Locate every blood parasite and identify its species.
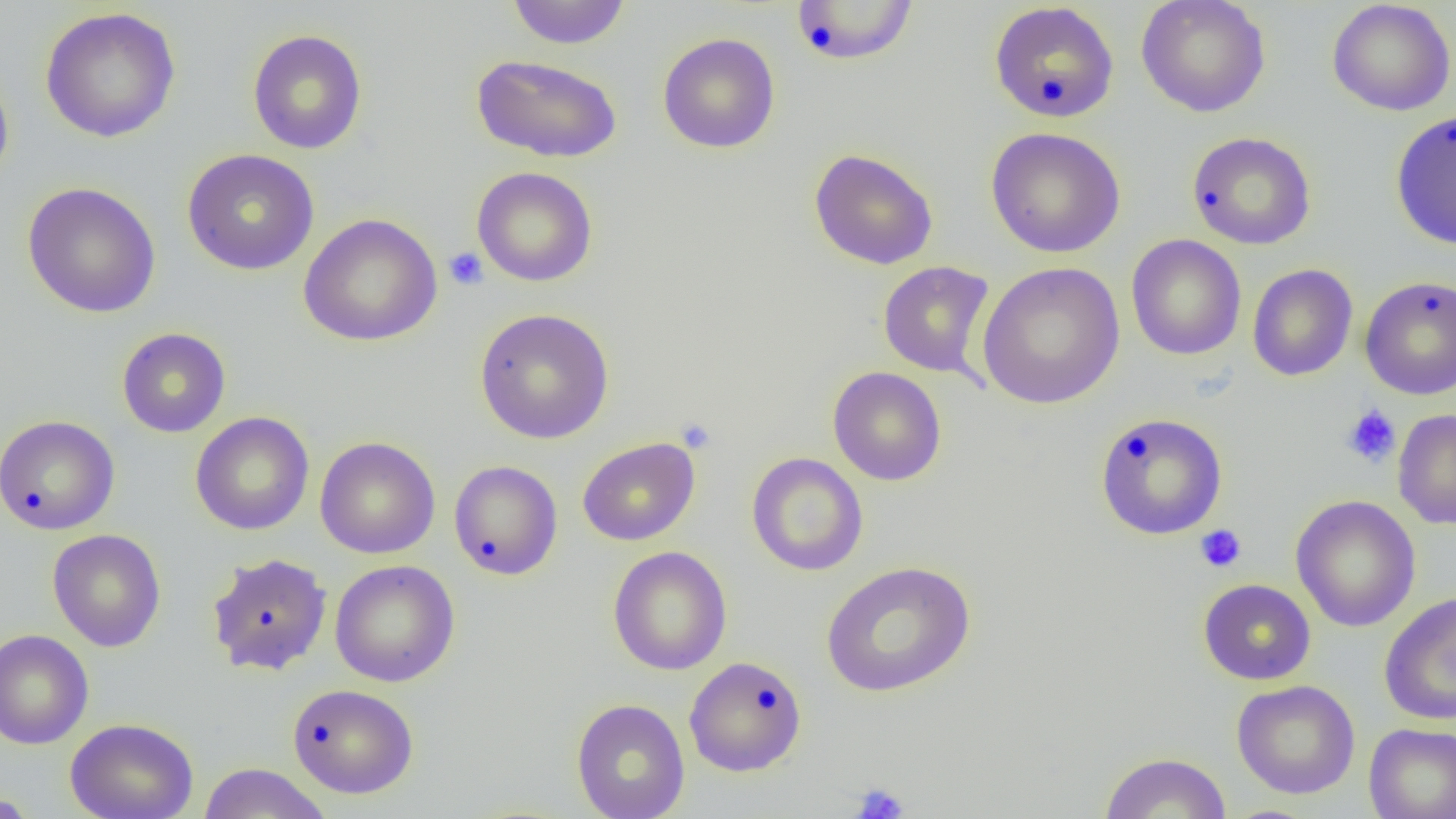

No blood parasites seen.

Approximate bounding boxes as (x1, y1, x2, y2) in pixels. Uninfected red blood cell locations: (506, 0, 631, 49), (1136, 0, 1271, 117), (1327, 0, 1456, 116), (790, 1, 920, 67), (989, 2, 1120, 123), (39, 7, 181, 143), (247, 28, 367, 155), (657, 32, 781, 153), (471, 53, 623, 163), (0, 64, 14, 188), (1390, 109, 1456, 250), (985, 127, 1126, 257), (1187, 131, 1316, 250), (182, 148, 320, 275), (809, 148, 938, 269), (471, 166, 598, 287), (22, 182, 161, 318), (298, 213, 443, 347), (1126, 234, 1246, 360), (878, 261, 995, 379), (977, 261, 1125, 410), (1247, 263, 1358, 381), (1359, 275, 1456, 400), (474, 308, 614, 444), (117, 328, 231, 437), (828, 367, 947, 486), (1393, 409, 1456, 529), (1094, 411, 1228, 540), (190, 412, 314, 535), (0, 415, 120, 535), (315, 437, 440, 559), (577, 437, 700, 546), (747, 452, 868, 576), (448, 460, 563, 580), (1290, 495, 1421, 632), (47, 529, 167, 652), (607, 546, 732, 676), (205, 552, 333, 676), (330, 559, 460, 687), (820, 560, 976, 698), (1198, 578, 1316, 685), (1379, 591, 1456, 726), (0, 629, 94, 749), (684, 656, 807, 777), (1231, 680, 1360, 799), (287, 683, 419, 798), (571, 698, 690, 819), (65, 717, 199, 819), (1363, 723, 1456, 819), (1099, 751, 1232, 818), (197, 762, 331, 819), (0, 791, 44, 817). Platelet locations: (443, 248, 488, 290), (1341, 405, 1401, 467), (675, 417, 716, 453), (1195, 524, 1246, 573), (851, 782, 909, 819). Slide-level diagnosis: negative for blood parasites. Thin blood smear. Captured at 1000x magnification. Single field of view. Image is 1456×819 pixels. Light microscopy.